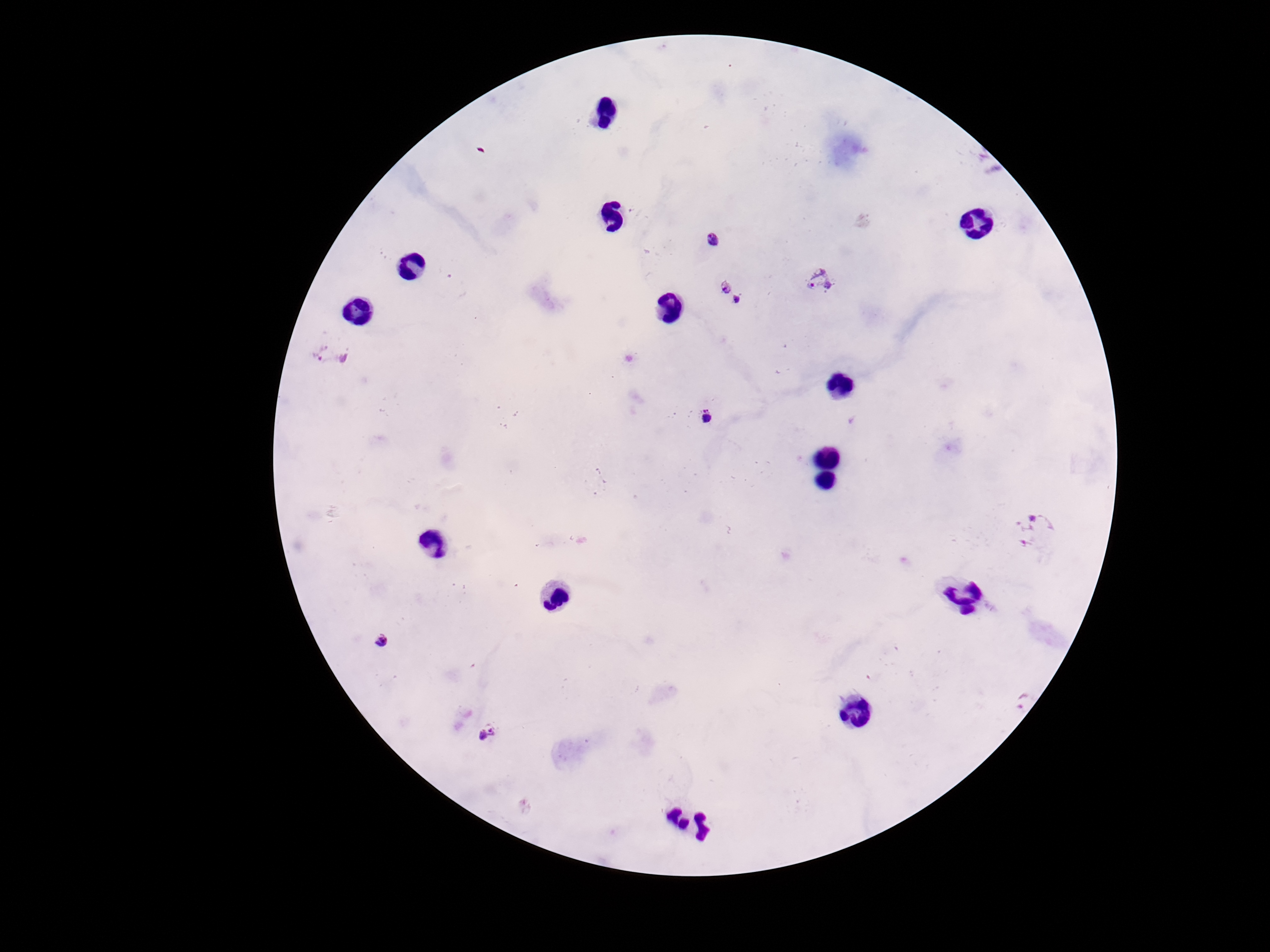

Approximate centers as (x, y) in pixels.
Summary:
  - Plasmodium parasite locations: (712, 241), (818, 281), (729, 292), (330, 354), (708, 420), (1035, 533), (379, 640), (1016, 694), (489, 732)
  - Capture: smartphone camera through the microscope eyepiece
  - Stain: Giemsa
  - Magnification: 100x
  - Image size: 1270×952 pixels
  - Patient malaria status: infected
  - Preparation: thick blood film
  - Field of view: single